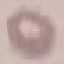
Malaria status: uninfected. Automatically extracted cell patch, resized to 64 × 64 pixels. Giemsa stain. Acquired by smartphone through the microscope eyepiece. Thin smear of blood.